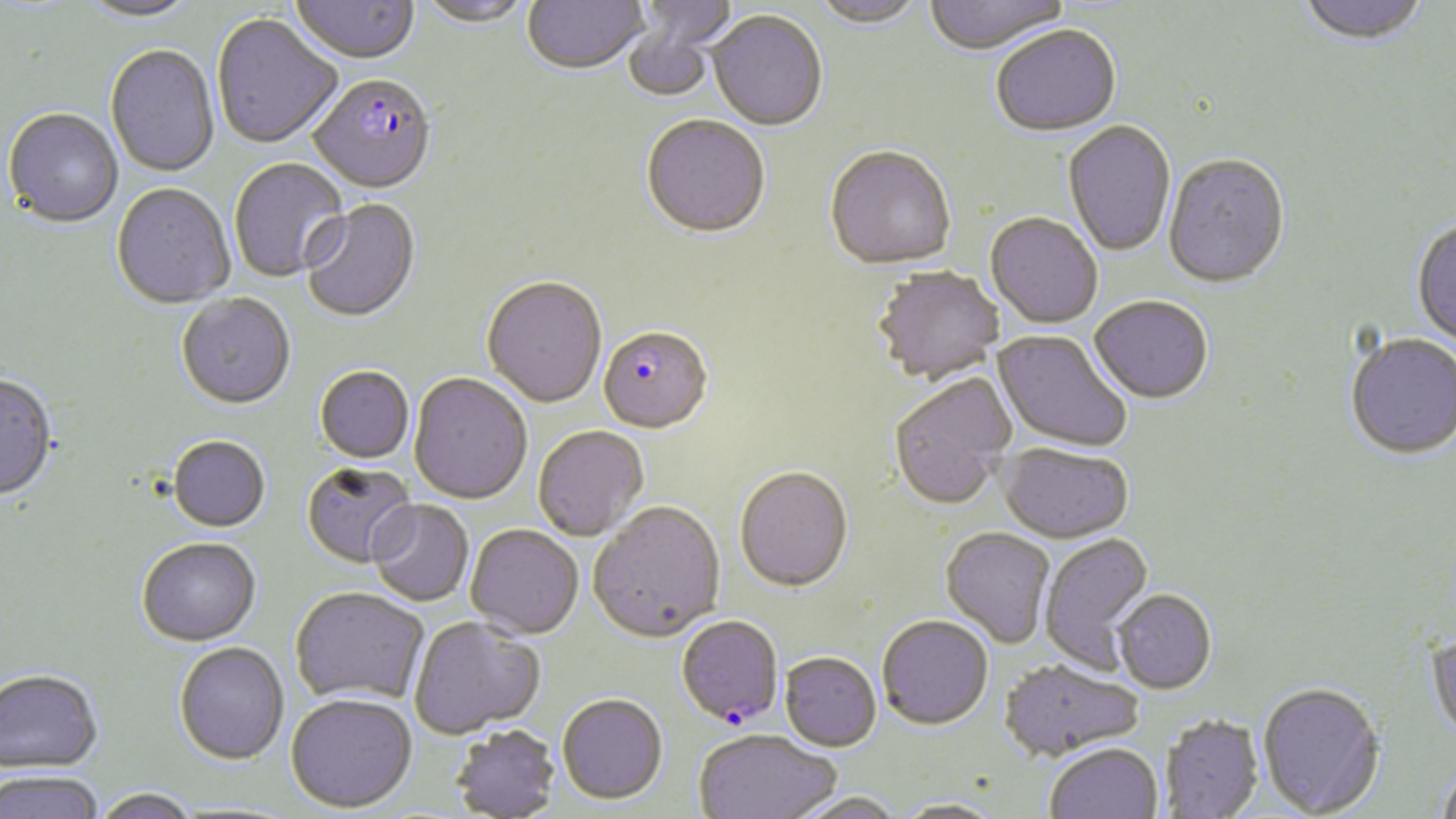
slide_level_diagnosis: Plasmodium falciparum
preparation: thin blood film
stain: May-Grünwald-Giemsa
uninfected_red_blood_cell_locations: 'approximate bounding boxes as (x1,y1)-(x2,y2) corner pairs in pixels: (290,0)-(420,66), (415,0)-(533,30), (523,0)-(648,77), (810,0)-(927,30), (923,0)-(1071,58), (1295,0)-(1431,48), (77,1)-(203,25), (635,1)-(740,49), (708,12)-(827,132), (212,16)-(343,151), (622,18)-(719,102), (991,26)-(1121,139), (105,46)-(220,178), (3,110)-(123,230), (641,117)-(770,241), (1063,122)-(1176,259), (824,148)-(957,273), (1163,156)-(1291,291), (230,159)-(350,282), (111,185)-(235,311), (300,200)-(421,323), (985,214)-(1102,329), (1411,218)-(1456,351), (872,266)-(1004,384), (481,278)-(607,409), (176,296)-(296,412), (1089,297)-(1214,405), (992,329)-(1132,454), (1345,333)-(1456,461), (315,367)-(415,464), (409,373)-(532,505), (888,374)-(1017,510), (0,376)-(58,502), (533,425)-(649,542), (168,437)-(270,533), (998,443)-(1133,543), (302,462)-(418,569), (734,467)-(853,593), (367,500)-(474,607), (589,502)-(727,644), (465,524)-(583,638), (940,527)-(1056,649), (1039,533)-(1155,672), (136,538)-(261,647), (290,586)-(429,707), (1113,589)-(1217,695), (877,615)-(993,731), (409,616)-(545,739), (1426,629)-(1456,749), (174,642)-(289,764), (780,652)-(881,752), (998,659)-(1144,761), (0,670)-(102,776), (1257,682)-(1386,817), (286,692)-(417,812), (557,694)-(668,805), (1159,714)-(1264,818), (448,725)-(561,818), (694,730)-(840,819), (1045,743)-(1163,819), (1437,766)-(1456,819), (0,772)-(104,819), (90,789)-(201,819), (788,792)-(905,819), (891,798)-(1008,818)'
magnification: 1000x
modality: light microscopy
image_size: 1456×819 pixels
field_of_view: one of a larger specimen
plasmodium_falciparum_infected_red_blood_cell_locations: 'approximate bounding boxes as (x1,y1)-(x2,y2) corner pairs in pixels: (309,76)-(437,196), (598,327)-(713,435), (676,615)-(784,726)'